Assess this cell for malaria.
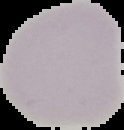

It is uninfected.

Summary:
  - Preparation: thin blood smear
  - Image size: 124×130 pixels
  - Image type: segmented cell region with the area outside set to black